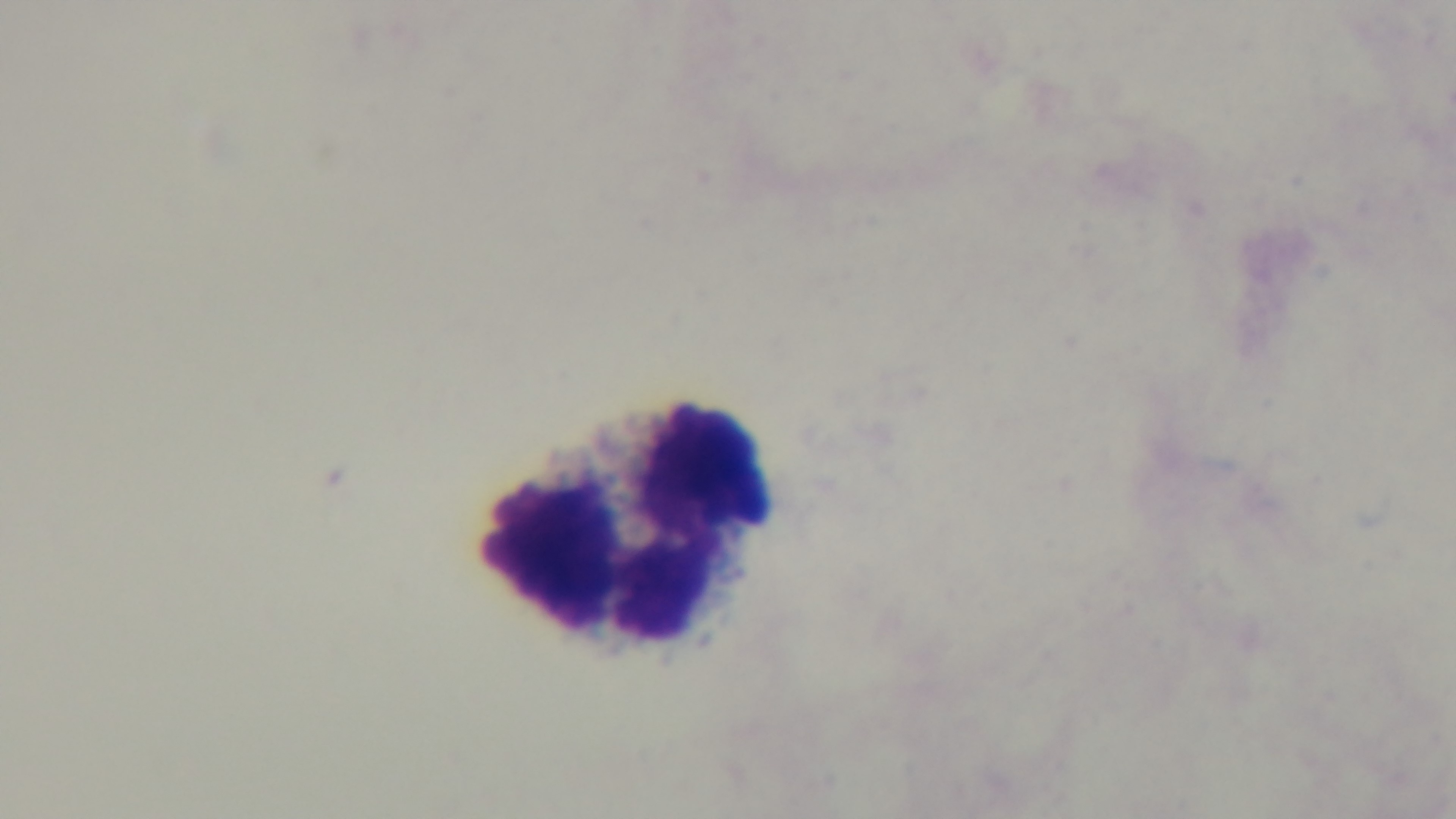 One field from the slide. Light microscopy. Malaria status: uninfected. Oil-immersion objective, 100x. Preparation: thick smear. Giemsa stain. Mounted 4K digital camera.